Point out each Plasmodium parasite.
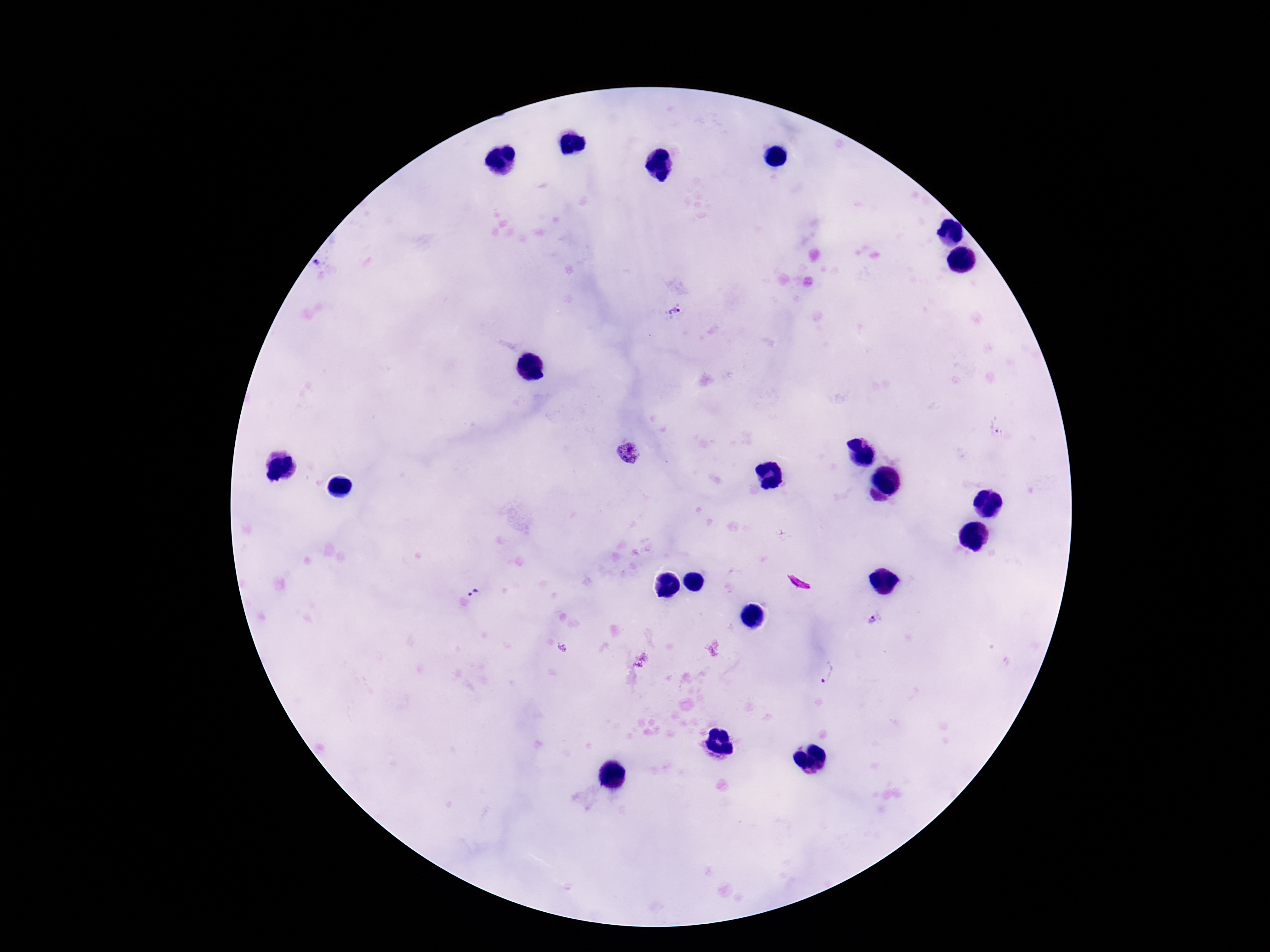
Approximate centers as (x, y) in pixels.
Plasmodium parasites: (319, 264), (675, 312), (998, 425), (627, 454), (475, 591), (872, 621), (828, 673).

Single field of view. Image is 1270×952 pixels. 100x magnification. Thick peripheral-blood smear. Patient malaria status: infected. Photographed through the microscope eyepiece with a smartphone camera. Giemsa stain.